Assess the morphology of the erythrocytes.
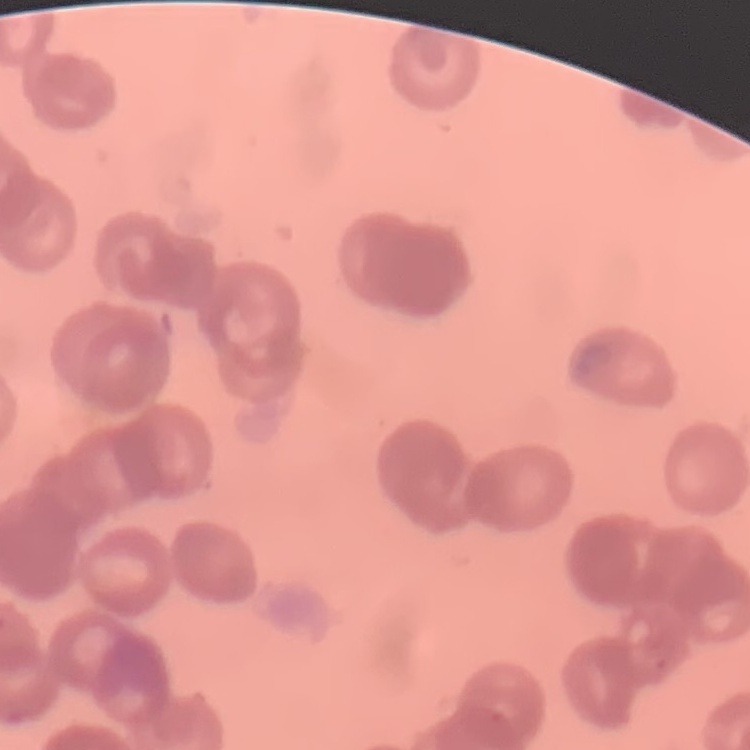

They show rouleaux formation.

Summary:
  - Preparation: thin peripheral smear
  - Stain: Field's or Giemsa
  - Image type: square crop of a larger photomicrograph